Assess for malaria.
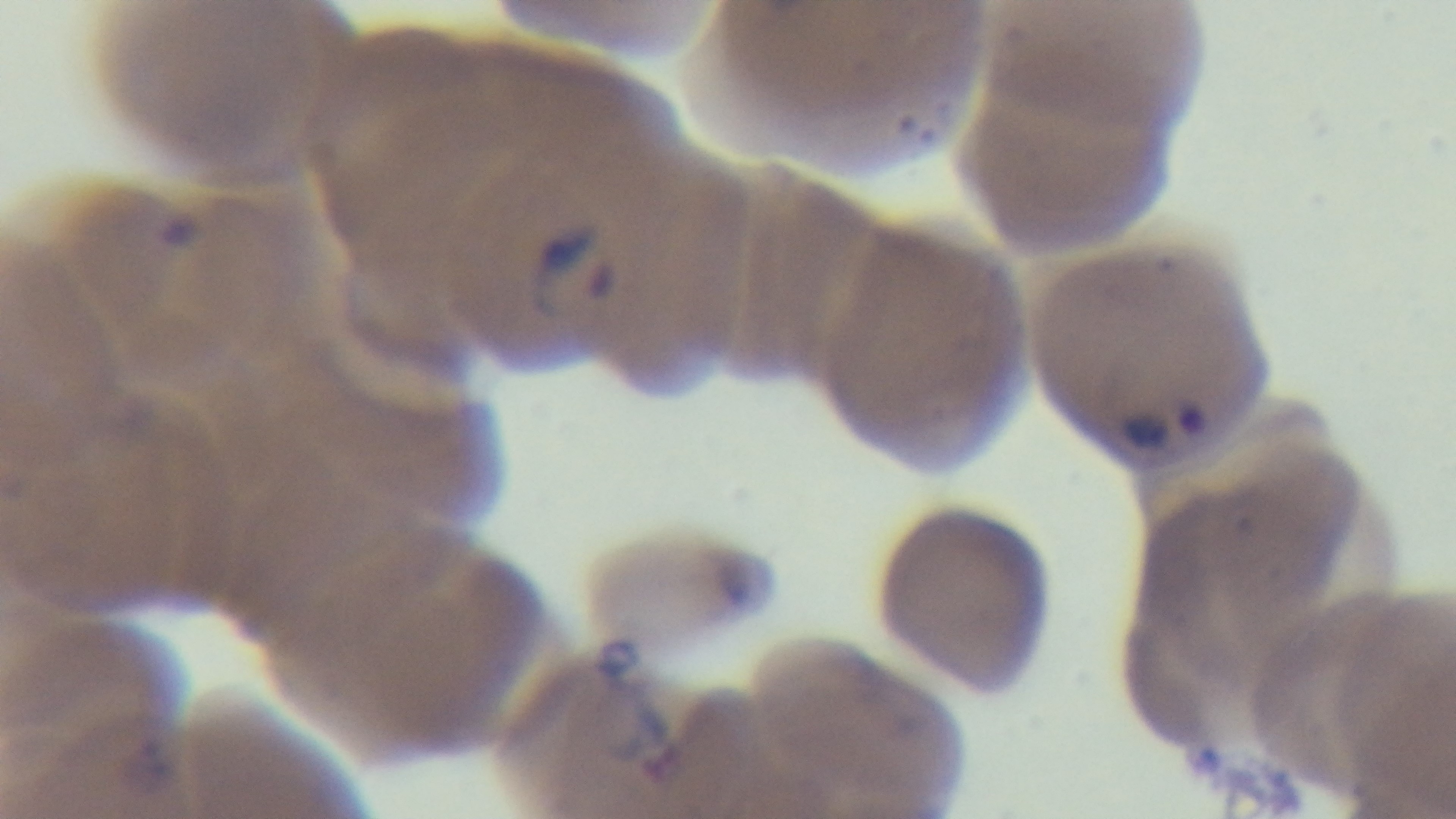

Infected.

Photomicrograph. One field from the slide. Giemsa stain. Preparation: thin smear. Captured with a mounted 4K digital camera. Oil-immersion objective, 100x.